Name the cell type shown.
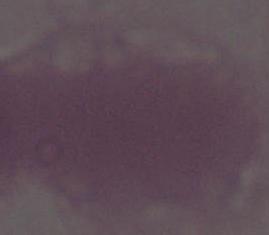
An erythrocyte.

magnification = 1000x
modality = micrograph